Assess the morphology of the red blood cells.
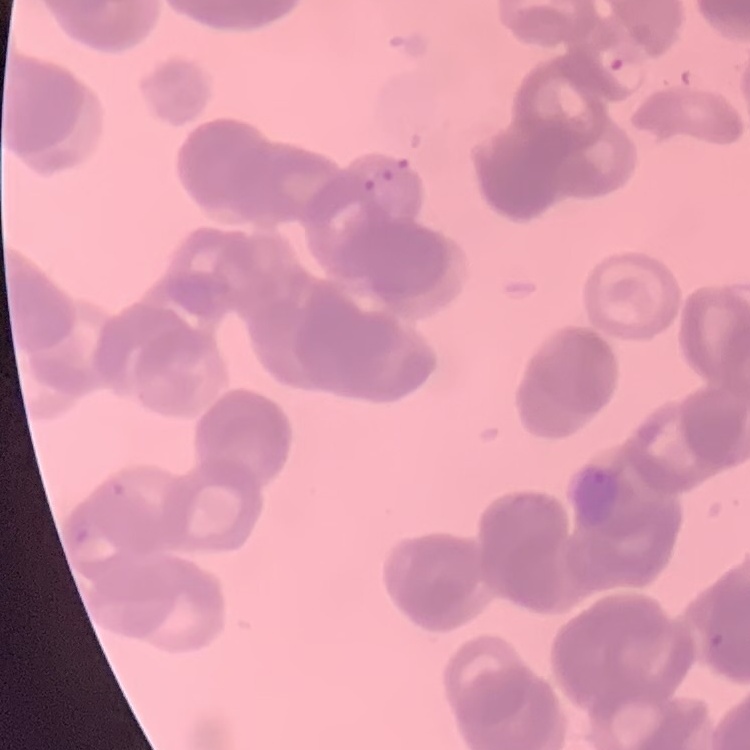
Rouleaux formation.

Stained with either Field's or Giemsa. Thin peripheral smear. Square crop of a larger photomicrograph.